Assess this cell for malaria.
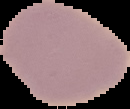

It is uninfected.

Summary:
  - Preparation: thin blood film
  - Image type: segmented cell region with the area outside set to black
  - Image size: 130×109 pixels